Assess this cell for malaria.
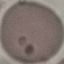

Uninfected.

image type = automatically extracted cell patch, resized to 64 × 64 pixels
preparation = thin blood smear
stain = Giemsa
capture = smartphone through the microscope eyepiece